Point out each malaria parasite and each leukocyte.
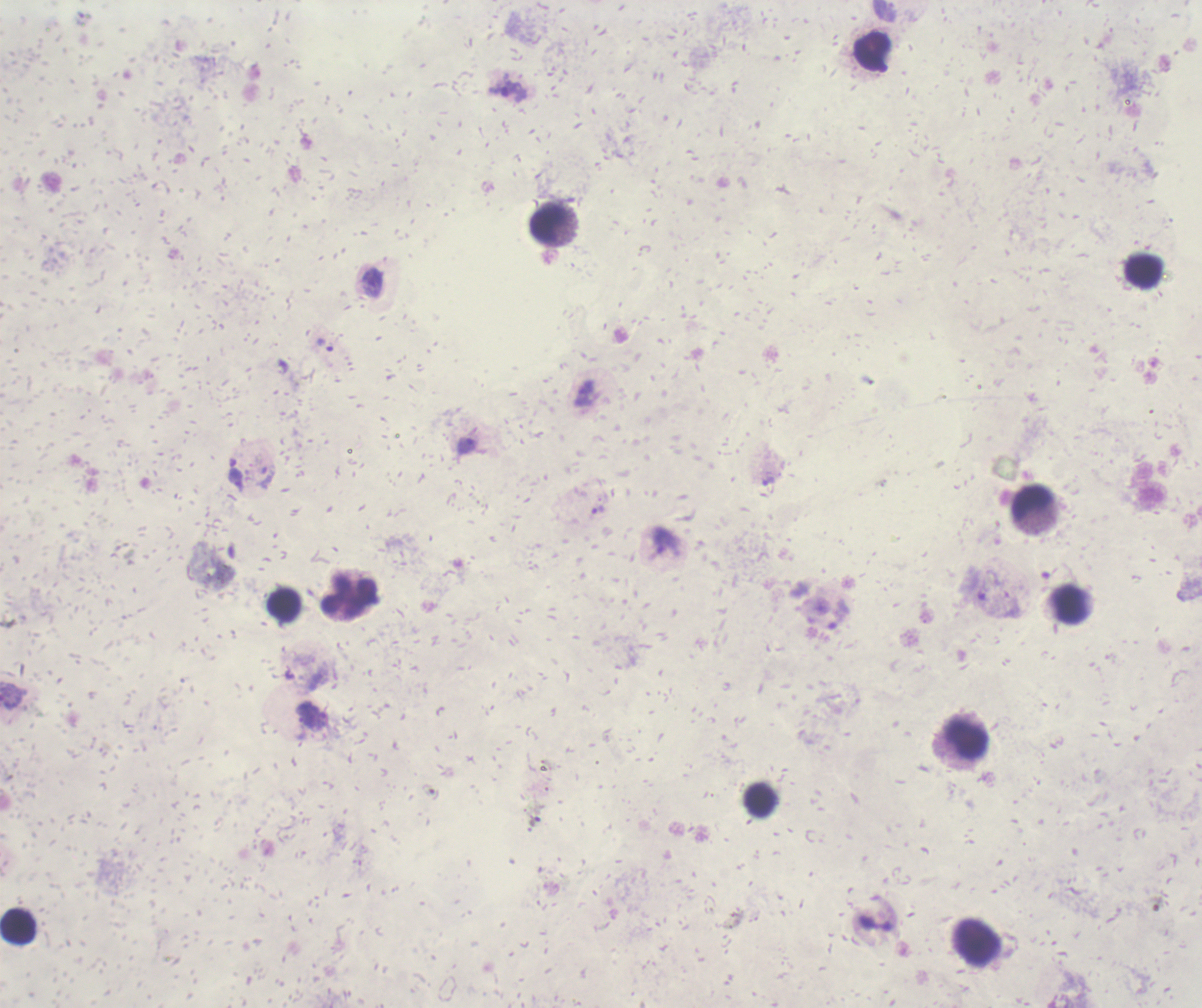
Approximate object centers, in pixels from the top-left corner.
Trophozoites: (x=508, y=90), (x=373, y=283), (x=325, y=345), (x=467, y=445), (x=769, y=481), (x=598, y=509), (x=838, y=614).
No schizont or gametocyte forms observed.
Leukocytes: (x=872, y=50), (x=547, y=222), (x=1143, y=271), (x=1032, y=502), (x=349, y=597), (x=1070, y=604), (x=284, y=605), (x=966, y=739), (x=760, y=800), (x=18, y=927).

context = previously used in an actual diagnosis
stain = Romanowsky
field of view = single
image size = 1202×1008 pixels
preparation = thick blood film
background quality = poor
coloration quality = bad
magnification = 100x